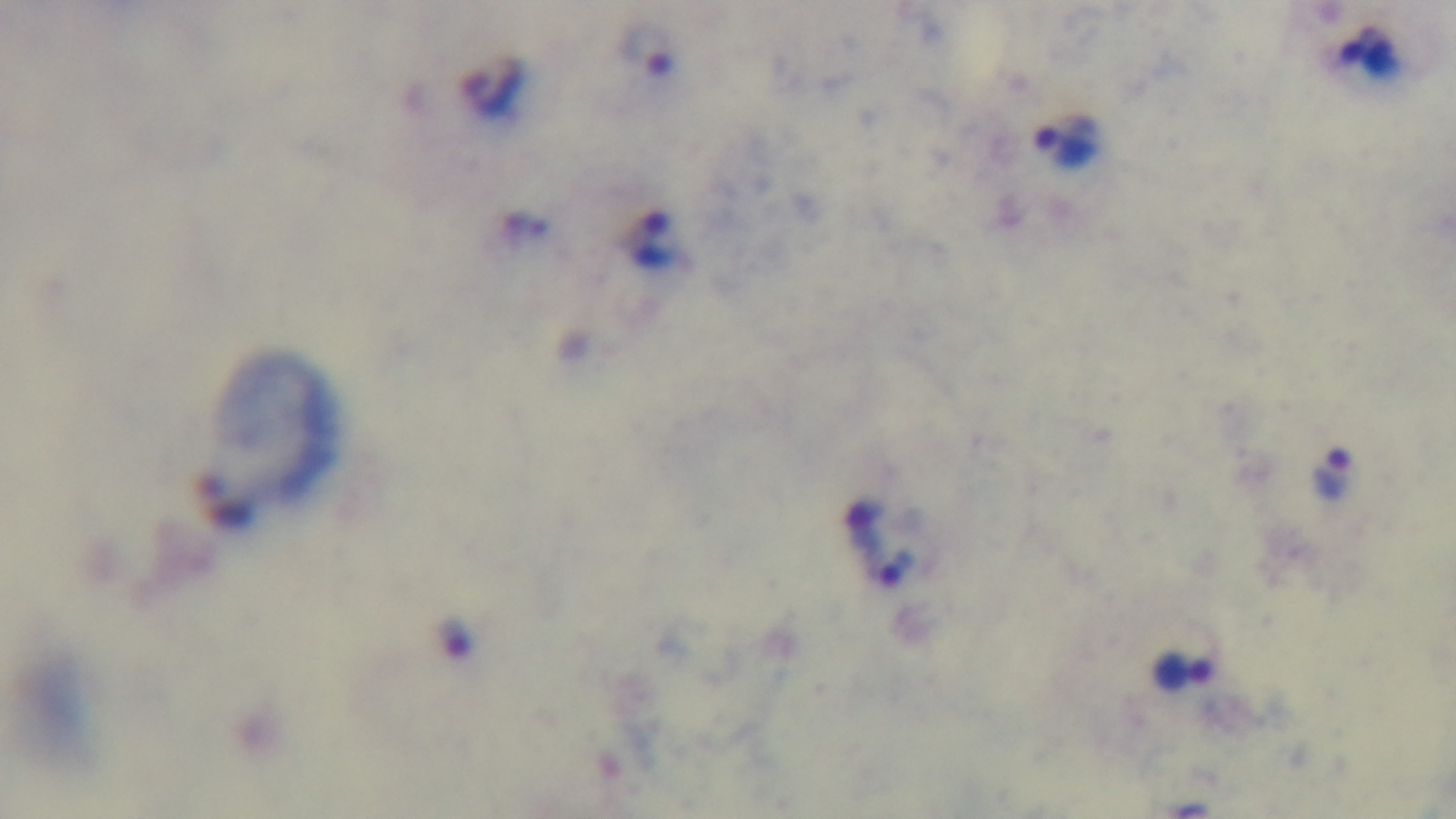 Captured with a mounted 4K digital camera. 100x oil-immersion objective. Single field of view. Giemsa-stained. Light microscopy. Preparation: thick. Malaria status: infected.